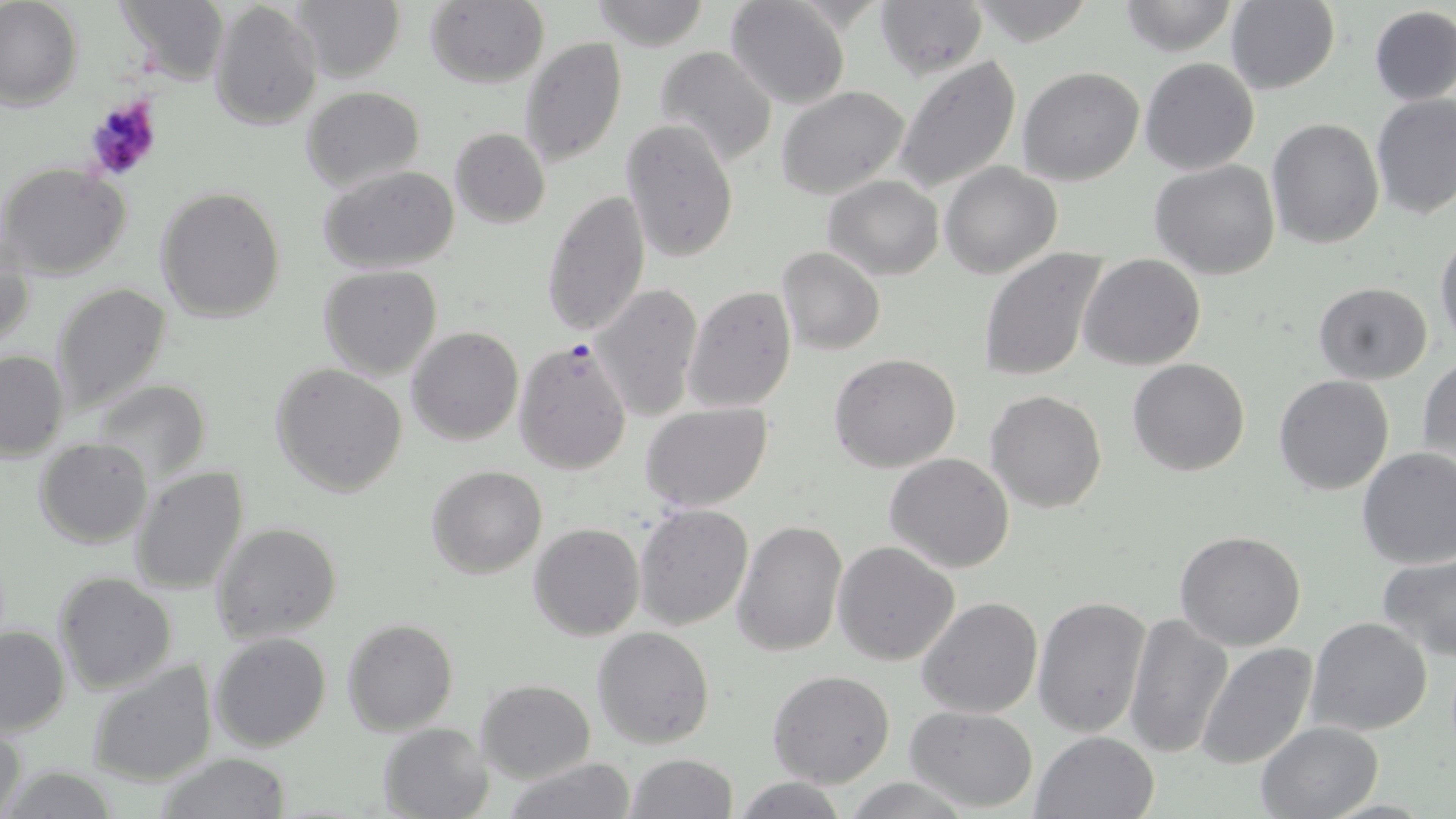

Summary:
  - Coordinate format: approximate bounding boxes as named x1/y1/x2/y2 corners in pixels
  - Uninfected red blood cell locations: (x1=0, y1=0, x2=84, y2=111), (x1=287, y1=0, x2=405, y2=84), (x1=589, y1=0, x2=710, y2=48), (x1=725, y1=0, x2=851, y2=109), (x1=875, y1=0, x2=989, y2=80), (x1=968, y1=0, x2=1097, y2=46), (x1=1117, y1=0, x2=1241, y2=56), (x1=111, y1=1, x2=229, y2=82), (x1=1225, y1=1, x2=1342, y2=96), (x1=207, y1=2, x2=322, y2=132), (x1=424, y1=2, x2=550, y2=88), (x1=1367, y1=5, x2=1456, y2=106), (x1=519, y1=38, x2=628, y2=171), (x1=654, y1=46, x2=779, y2=167), (x1=893, y1=55, x2=1022, y2=196), (x1=1140, y1=56, x2=1260, y2=175), (x1=1017, y1=67, x2=1146, y2=185), (x1=300, y1=85, x2=425, y2=193), (x1=777, y1=85, x2=912, y2=199), (x1=1372, y1=96, x2=1456, y2=221), (x1=1267, y1=116, x2=1384, y2=250), (x1=619, y1=118, x2=739, y2=264), (x1=448, y1=127, x2=550, y2=228), (x1=1150, y1=159, x2=1281, y2=281), (x1=940, y1=162, x2=1064, y2=279), (x1=1, y1=164, x2=132, y2=281), (x1=318, y1=165, x2=461, y2=275), (x1=822, y1=175, x2=945, y2=279), (x1=541, y1=187, x2=650, y2=338), (x1=156, y1=188, x2=286, y2=323), (x1=1435, y1=233, x2=1456, y2=347), (x1=1, y1=236, x2=33, y2=355), (x1=776, y1=247, x2=886, y2=356), (x1=976, y1=247, x2=1107, y2=383), (x1=1078, y1=255, x2=1204, y2=371), (x1=318, y1=265, x2=443, y2=380), (x1=1313, y1=282, x2=1434, y2=384), (x1=51, y1=283, x2=173, y2=417), (x1=591, y1=283, x2=704, y2=421), (x1=685, y1=285, x2=797, y2=413), (x1=406, y1=326, x2=523, y2=446), (x1=0, y1=348, x2=70, y2=459), (x1=829, y1=353, x2=961, y2=473), (x1=1126, y1=357, x2=1252, y2=476), (x1=1418, y1=358, x2=1456, y2=471), (x1=271, y1=364, x2=408, y2=499), (x1=1273, y1=373, x2=1395, y2=495), (x1=92, y1=379, x2=212, y2=484), (x1=986, y1=390, x2=1108, y2=513), (x1=641, y1=403, x2=773, y2=513), (x1=34, y1=438, x2=154, y2=549), (x1=1356, y1=446, x2=1456, y2=569), (x1=884, y1=453, x2=1015, y2=574), (x1=130, y1=465, x2=250, y2=595), (x1=426, y1=465, x2=547, y2=580), (x1=633, y1=503, x2=754, y2=631), (x1=732, y1=518, x2=848, y2=657), (x1=211, y1=522, x2=343, y2=643), (x1=529, y1=522, x2=644, y2=641), (x1=1174, y1=530, x2=1307, y2=651), (x1=833, y1=540, x2=960, y2=666), (x1=1377, y1=552, x2=1456, y2=663), (x1=53, y1=571, x2=180, y2=696), (x1=1031, y1=595, x2=1151, y2=739), (x1=915, y1=597, x2=1042, y2=719), (x1=1122, y1=612, x2=1231, y2=761), (x1=342, y1=618, x2=457, y2=735), (x1=1306, y1=618, x2=1433, y2=737), (x1=0, y1=625, x2=70, y2=736), (x1=592, y1=626, x2=715, y2=749), (x1=210, y1=632, x2=331, y2=752), (x1=1195, y1=642, x2=1319, y2=771), (x1=88, y1=658, x2=218, y2=787), (x1=767, y1=671, x2=896, y2=789), (x1=477, y1=680, x2=594, y2=782), (x1=904, y1=706, x2=1038, y2=812), (x1=1, y1=720, x2=28, y2=819), (x1=1254, y1=720, x2=1386, y2=818), (x1=377, y1=722, x2=492, y2=819), (x1=1031, y1=729, x2=1160, y2=819), (x1=153, y1=753, x2=293, y2=819), (x1=625, y1=754, x2=739, y2=818), (x1=502, y1=760, x2=640, y2=818), (x1=732, y1=777, x2=850, y2=818)
  - Plasmodium falciparum-infected red blood cell locations: (x1=513, y1=338, x2=634, y2=474)
  - Platelet locations: (x1=80, y1=94, x2=165, y2=185)
  - Slide-level diagnosis: Plasmodium falciparum
  - Modality: light microscopy
  - Preparation: thin blood film
  - Magnification: 1000x
  - Field of view: one of a larger specimen
  - Image size: 1456×819 pixels
  - Stain: May-Grünwald-Giemsa